State which parasite is depicted.
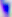
Toxoplasma gondii.

{
  "magnification": "400x",
  "modality": "photomicrograph"
}